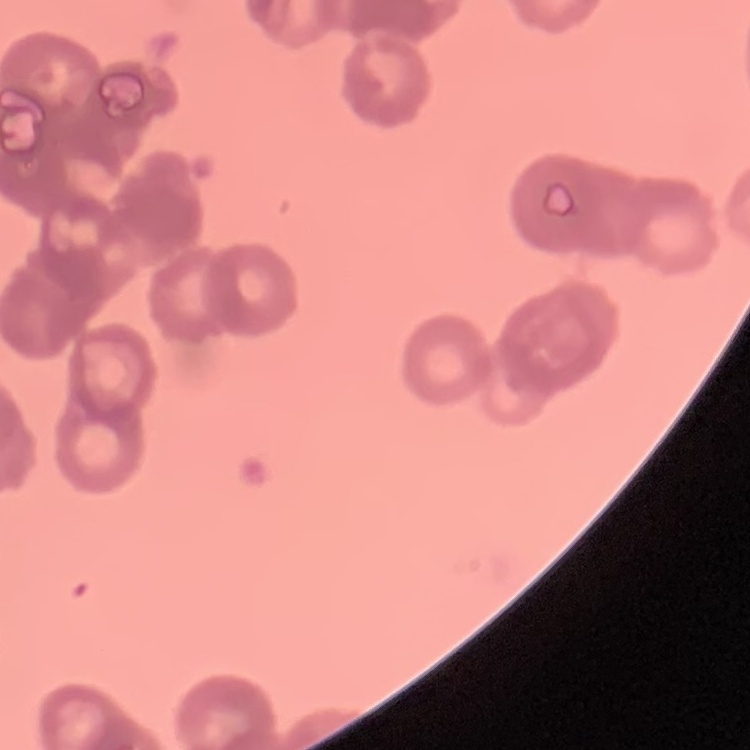
Summary:
  - Red blood cell morphology: rouleaux formation
  - Preparation: thin peripheral smear
  - Image type: one tile cut from a larger photomicrograph
  - Stain: Field's or Giemsa